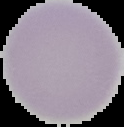
Image is 124×127 pixels. Malaria status: uninfected. Segmented cell region on a black background. From a thin blood smear.